Identify the blood parasite species.
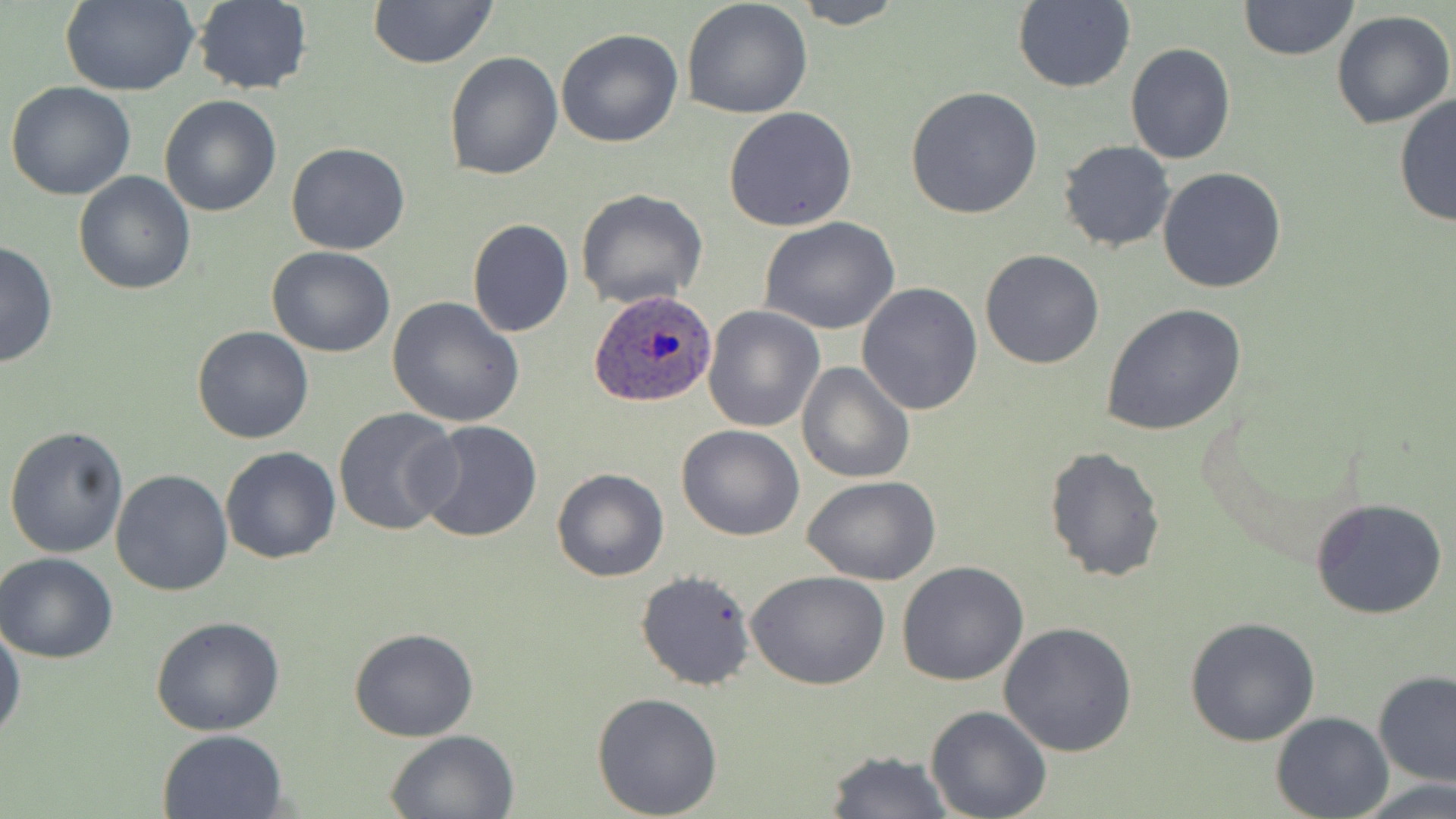
Plasmodium ovale.

Approximate bounding boxes as (x1, y1, x2, y2) in pixels. Uninfected red blood cell locations: (365, 0, 499, 69), (682, 0, 813, 118), (787, 0, 907, 29), (59, 1, 199, 95), (190, 1, 312, 96), (1010, 1, 1136, 92), (1238, 1, 1361, 63), (1330, 10, 1455, 129), (555, 27, 685, 148), (1124, 43, 1236, 165), (444, 51, 563, 180), (6, 81, 137, 200), (903, 84, 1044, 219), (1394, 92, 1455, 231), (159, 94, 282, 217), (723, 106, 858, 231), (1057, 140, 1176, 253), (286, 142, 412, 255), (1157, 166, 1287, 293), (74, 171, 196, 295), (575, 189, 708, 309), (759, 218, 901, 334), (467, 219, 574, 337), (0, 241, 58, 371), (267, 246, 396, 359), (979, 248, 1106, 368), (856, 283, 983, 415), (388, 296, 526, 427), (1101, 302, 1249, 437), (701, 303, 826, 433), (190, 327, 313, 445), (796, 361, 916, 484), (333, 407, 462, 539), (414, 420, 543, 544), (4, 424, 130, 559), (676, 424, 805, 542), (1043, 445, 1167, 583), (221, 447, 342, 564), (553, 468, 669, 582), (110, 469, 234, 596), (803, 476, 941, 585), (1308, 496, 1450, 621), (0, 552, 119, 663), (897, 561, 1029, 685), (635, 569, 757, 691), (746, 570, 890, 690), (151, 616, 285, 736), (1184, 616, 1321, 746), (0, 619, 23, 744), (1000, 622, 1137, 757), (349, 627, 479, 741), (1373, 669, 1456, 788), (591, 692, 723, 818), (926, 705, 1052, 819), (1271, 711, 1394, 819), (157, 728, 288, 818), (385, 730, 519, 817), (825, 749, 950, 818), (1357, 778, 1456, 817). Plasmodium ovale-infected red blood cell locations: (588, 288, 720, 408). 1000x magnification. Image is 1456×819 pixels. One field of a larger specimen. Light microscopy. May-Grünwald-Giemsa-stained preparation. Thin blood film.